Give the position of every leukocyte visible.
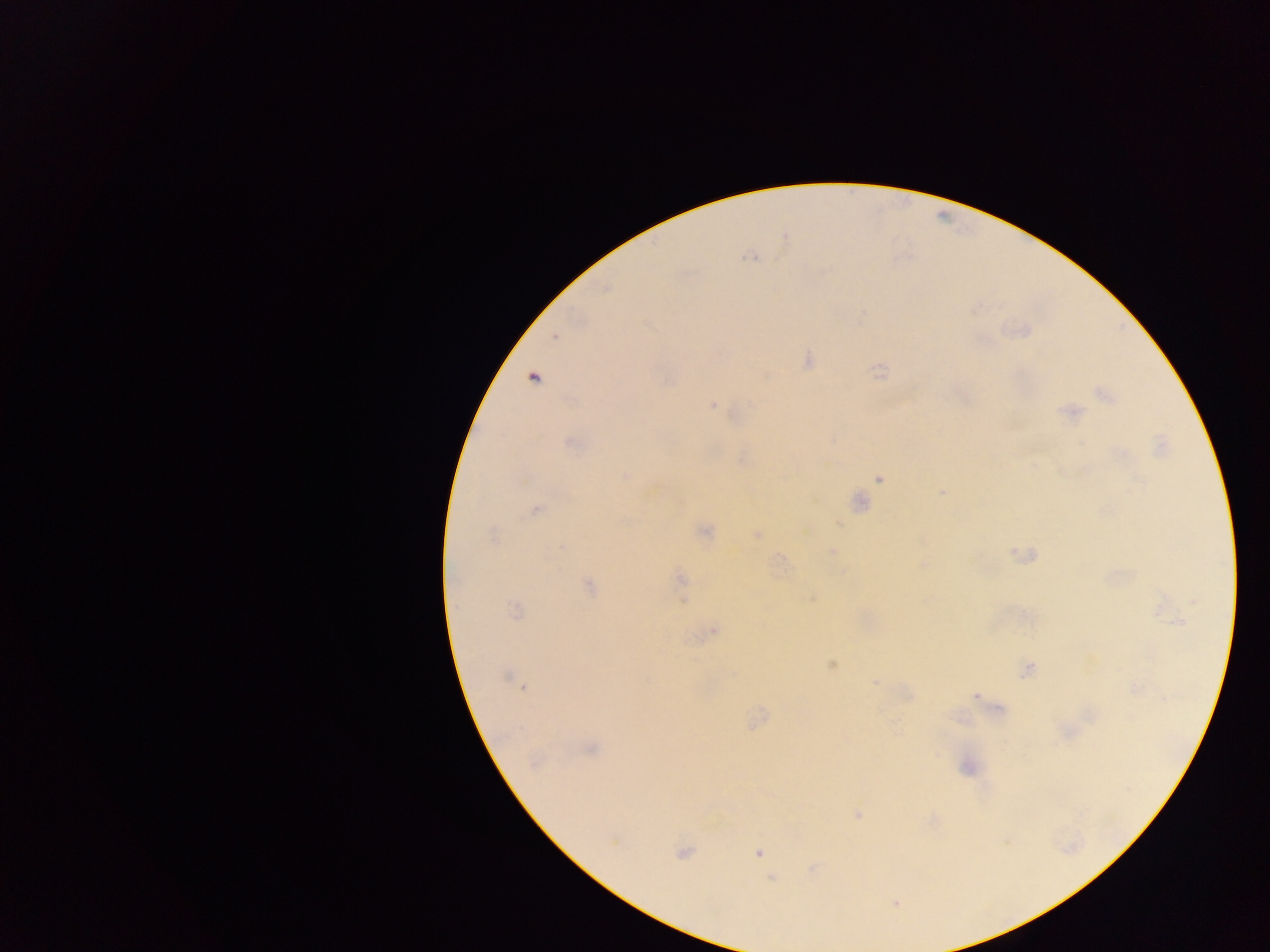
No leukocytes observed.

Approximate centers as {x, y} in pixels. Malaria parasite locations: {750, 256}, {555, 336}, {808, 359}, {880, 372}, {533, 378}, {1104, 395}, {713, 406}, {1071, 413}, {569, 442}, {1161, 446}, {880, 477}, {941, 492}, {857, 502}, {536, 509}, {704, 531}, {492, 535}, {757, 535}, {831, 552}, {923, 564}, {681, 579}, {588, 587}, {811, 597}, {514, 610}, {712, 630}, {830, 663}, {1029, 670}, {509, 677}, {876, 681}, {976, 695}, {756, 720}, {588, 749}, {534, 762}, {967, 766}, {858, 815}, {682, 851}, {757, 852}, {812, 868}, {772, 879}, {895, 903}. Mobile-phone photograph taken through the microscope. Image is 1270×952 pixels. Collected in Ghana. Thick blood smear. Single field of view.